Assess this cell for malaria.
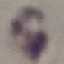
It is uninfected.

Thin smear of blood. Giemsa stain. Photographed with a smartphone camera at the microscope eyepiece. Automatically extracted cell patch, resized to 64 × 64 pixels.